Assess this cell for malaria.
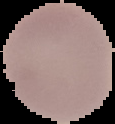
It is uninfected.

Segmented cell region on a black background. From a thin blood film. Image is 115×124 pixels.